Comment on the morphology of the erythrocytes.
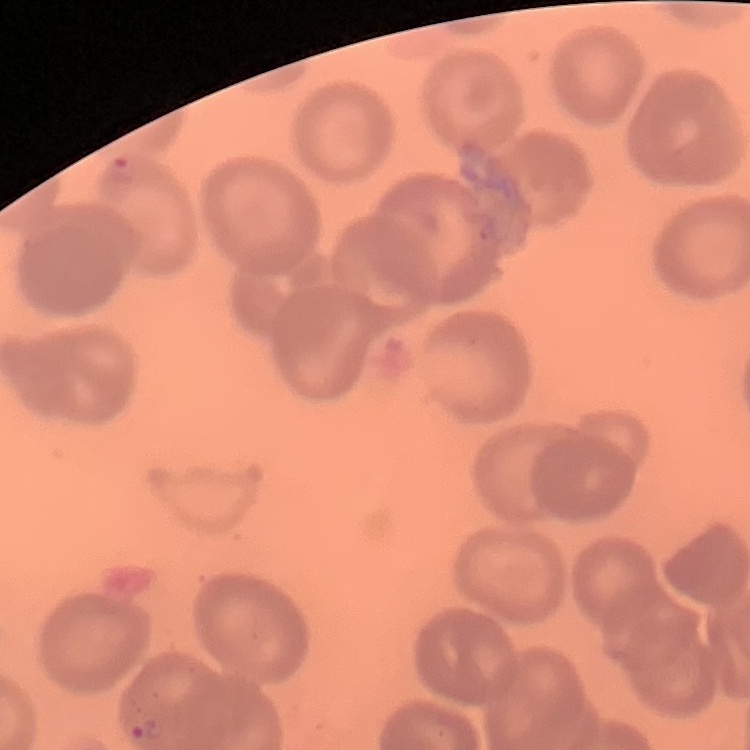

They show no rouleaux formation.

{
  "stain": "Field's or Giemsa",
  "preparation": "thin blood film",
  "image_type": "one tile cut from a larger photomicrograph"
}